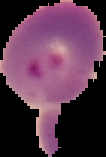
malaria_status: parasitized
image_size: 106×157 pixels
preparation: thin blood smear
image_type: segmented cell region with the area outside set to black